Assess this cell for malaria.
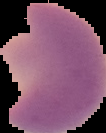

Parasitized.

From a thin blood film. Segmented cell region on a black background. Image is 106×133 pixels.